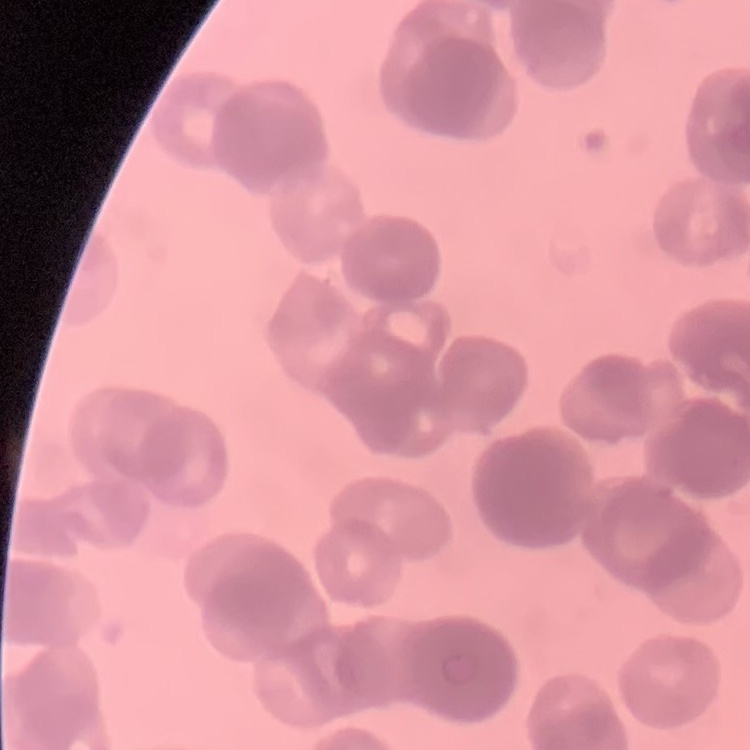
{
  "red_blood_cell_morphology": "rouleaux formation",
  "preparation": "thin peripheral smear",
  "stain": "Field's or Giemsa",
  "image_type": "square crop of a larger photomicrograph"
}